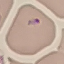

Summary:
  - Result: malaria parasites detected
  - Capture: smartphone through the microscope eyepiece
  - Stain: Giemsa
  - Preparation: thin blood film
  - Image type: automatically extracted cell patch, resized to 64 × 64 pixels